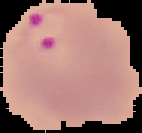

Summary:
  - Malaria status: parasitized
  - Preparation: thin blood smear
  - Image size: 142×133 pixels
  - Image type: segmented cell region on a black background